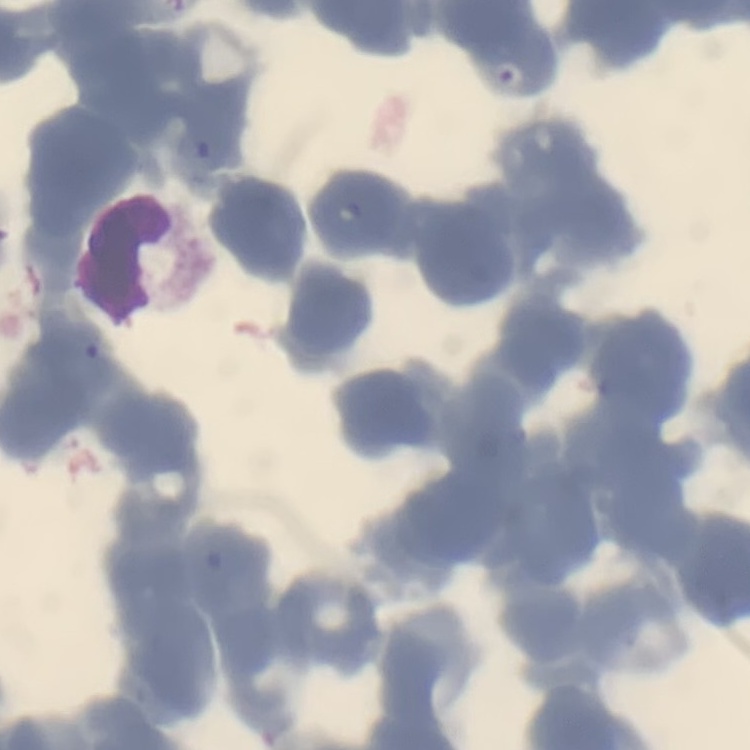

Summary:
  - Erythrocyte morphology: rouleaux formation
  - Image type: one tile cut from a larger photomicrograph
  - Stain: Field's or Giemsa
  - Preparation: thin blood film